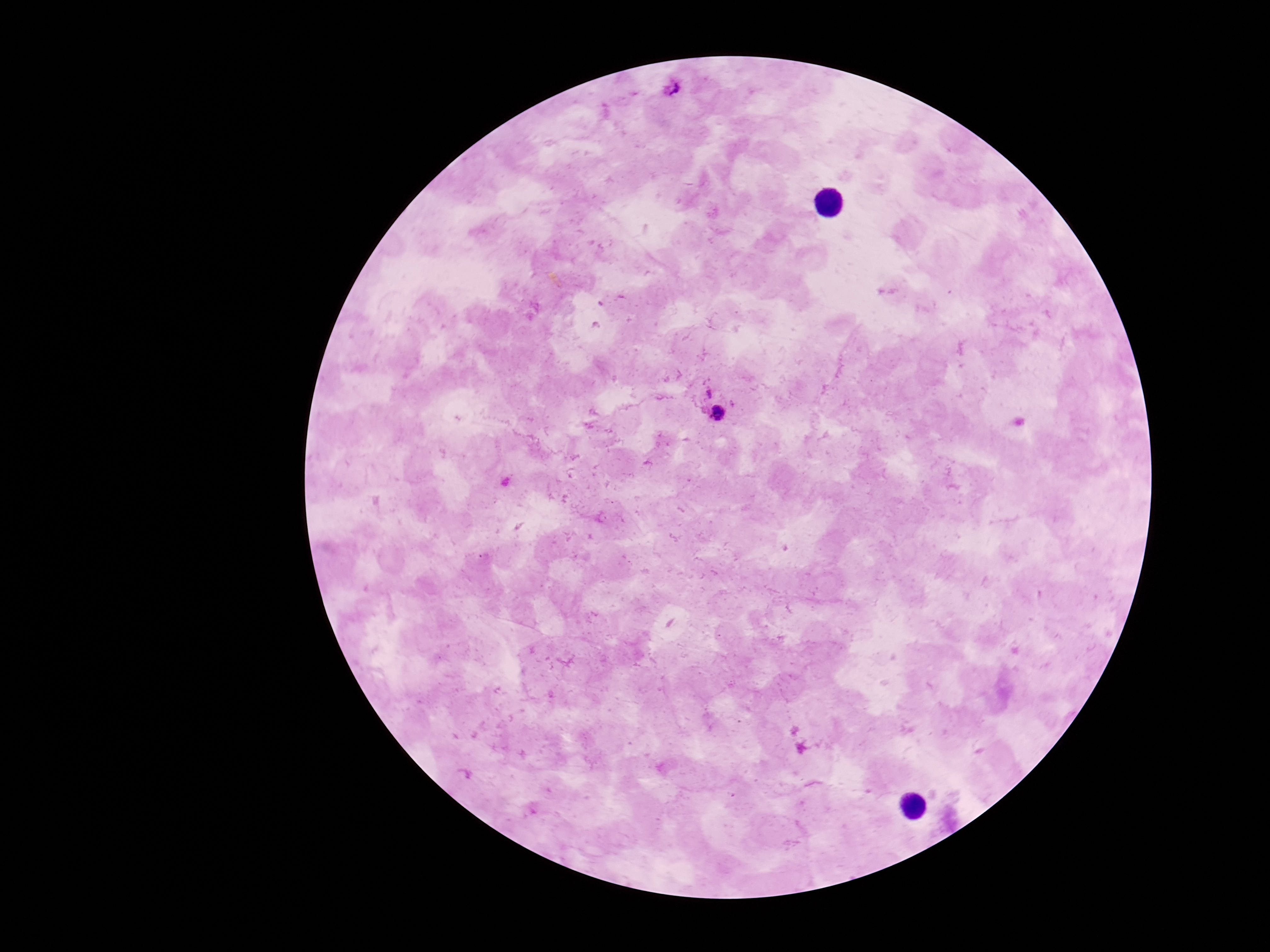
patient malaria status = positive
preparation = thick blood smear
image size = 1270×952 pixels
field of view = one from this slide
magnification = 100x
stain = Giemsa
Plasmodium parasite locations = approximate centers as {x, y} in pixels: {673, 90}, {718, 406}
capture = smartphone camera through the microscope eyepiece